Report the malaria status of this cell.
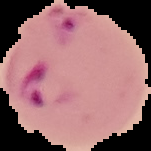

Parasitized.

From a thin blood smear. Image is 151×151 pixels. Cell region segmented out of the field of view; the surrounding area is masked to black.